Report the malaria status of this cell.
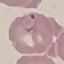

Parasitized.

image type = cell patch, automatically extracted from a larger field of view and resized to 64 × 64 pixels
capture = smartphone through the microscope eyepiece
preparation = thin blood film
stain = Giemsa